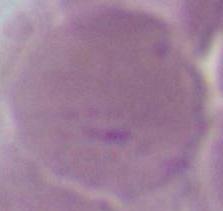
An erythrocyte is seen. Micrograph. 1000x magnification.